Classify this cell by malaria status.
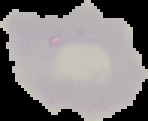

It is uninfected.

Summary:
  - Image size: 148×121 pixels
  - Image type: segmented cell region on a black background
  - Preparation: thin blood film